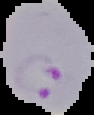

image_type: cell region segmented out of the field of view; surrounding area masked to black
result: malaria parasites detected
preparation: thin blood smear
image_size: 94×115 pixels